Outline each Trypanosoma brucei.
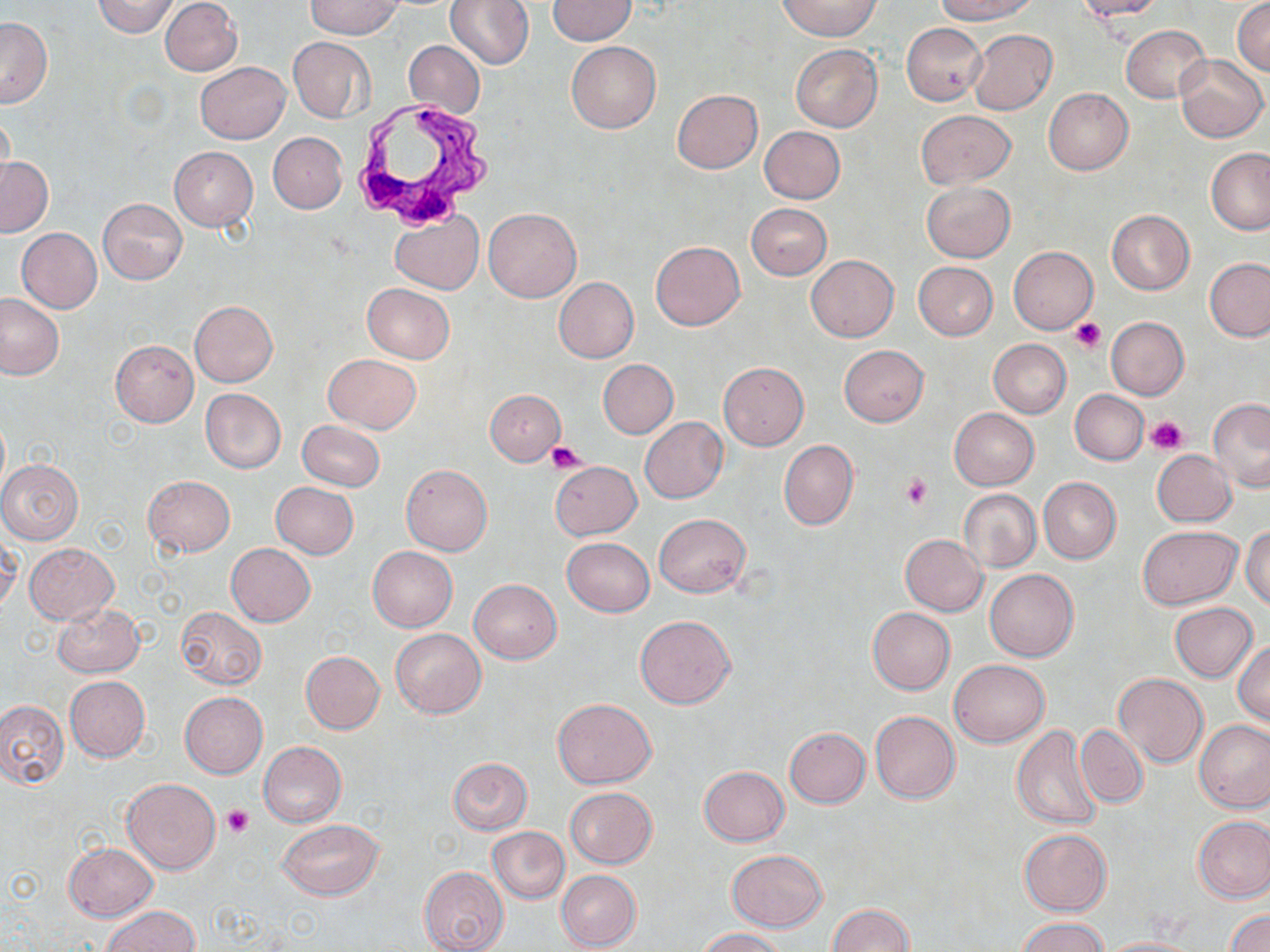

Approximate bounding boxes as (x1,y1)-(x2,y2) corner pairs in pixels.
Trypanosoma brucei: (352,99)-(489,229).

slide-level diagnosis = Trypanosoma brucei
preparation = thin blood smear
modality = optical microscopy
uninfected red blood cell locations = approximate bounding boxes as (x1,y1)-(x2,y2) corner pairs in pixels: (93,0)-(179,37), (160,0)-(242,76), (305,0)-(403,39), (445,0)-(534,69), (547,0)-(636,45), (778,0)-(882,40), (934,0)-(1036,24), (1073,0)-(1165,20), (1232,0)-(1270,76), (0,18)-(51,107), (901,22)-(987,104), (1120,25)-(1211,103), (968,29)-(1057,115), (289,37)-(374,122), (404,40)-(484,119), (565,41)-(661,133), (791,44)-(881,131), (1175,55)-(1267,142), (195,61)-(290,143), (1043,88)-(1133,175), (672,89)-(762,173), (1,106)-(15,195), (915,109)-(1015,188), (758,125)-(846,204), (268,132)-(347,214), (168,146)-(258,230), (1206,150)-(1270,233), (1,157)-(52,238), (922,181)-(1015,262), (98,198)-(187,284), (747,203)-(831,280), (484,208)-(582,302), (1106,209)-(1194,294), (391,214)-(482,293), (17,228)-(102,313), (651,242)-(745,329), (1008,246)-(1097,333), (806,255)-(898,342), (1204,257)-(1270,341), (914,262)-(997,340), (553,277)-(639,363), (362,283)-(455,363), (0,293)-(63,380), (188,301)-(278,386), (1105,317)-(1189,400), (988,339)-(1070,417), (111,341)-(199,426), (839,345)-(929,426), (323,353)-(421,433), (599,359)-(677,438), (718,362)-(809,451), (200,388)-(286,473), (486,389)-(565,465), (1070,389)-(1148,465), (1208,399)-(1270,492), (949,408)-(1039,489), (640,417)-(727,503), (297,420)-(385,492), (779,439)-(859,530), (1152,449)-(1236,527), (0,460)-(83,544), (551,461)-(641,539), (401,464)-(492,557), (142,476)-(235,557), (1039,477)-(1121,563), (270,482)-(358,559), (959,489)-(1041,573), (654,513)-(751,597), (1138,525)-(1241,609), (1242,526)-(1270,609), (0,532)-(20,614), (900,534)-(988,616), (562,536)-(654,616), (23,542)-(118,624), (226,543)-(315,627), (368,547)-(457,631), (985,569)-(1079,662), (468,579)-(562,663), (1169,601)-(1258,682), (52,604)-(145,678), (176,606)-(266,690), (867,607)-(954,695), (635,615)-(736,708), (391,628)-(487,718), (1234,639)-(1270,726), (300,651)-(385,734), (950,659)-(1049,747), (1113,673)-(1209,768), (65,675)-(150,762), (180,692)-(267,777), (553,698)-(657,787), (0,699)-(69,789), (869,711)-(961,804), (1195,719)-(1270,812), (1012,724)-(1103,829), (1076,724)-(1149,809), (785,727)-(870,807), (258,741)-(348,827), (448,757)-(532,834), (698,765)-(789,847), (122,778)-(220,874), (564,787)-(658,867), (1194,816)-(1270,903), (278,818)-(383,899), (486,826)-(570,904), (1019,829)-(1111,915), (63,843)-(159,922), (727,849)-(827,931), (419,865)-(509,952), (557,869)-(642,951), (826,904)-(913,952), (104,906)-(199,952), (1226,910)-(1270,952), (1016,916)-(1110,952), (695,928)-(786,951), (1095,937)-(1207,952)
stain = May-Grünwald-Giemsa
platelet locations = approximate bounding boxes as (x1,y1)-(x2,y2) corner pairs in pixels: (1070,318)-(1107,352), (1146,415)-(1187,454), (546,442)-(585,472), (901,474)-(932,509), (222,804)-(254,837)
field of view = one of a larger specimen
image size = 1270×952 pixels
magnification = 1000x